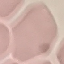
malaria_status: uninfected
capture: smartphone through the microscope eyepiece
stain: Giemsa
preparation: thin blood film
image_type: cell patch, automatically extracted from a larger field of view and resized to 64 × 64 pixels